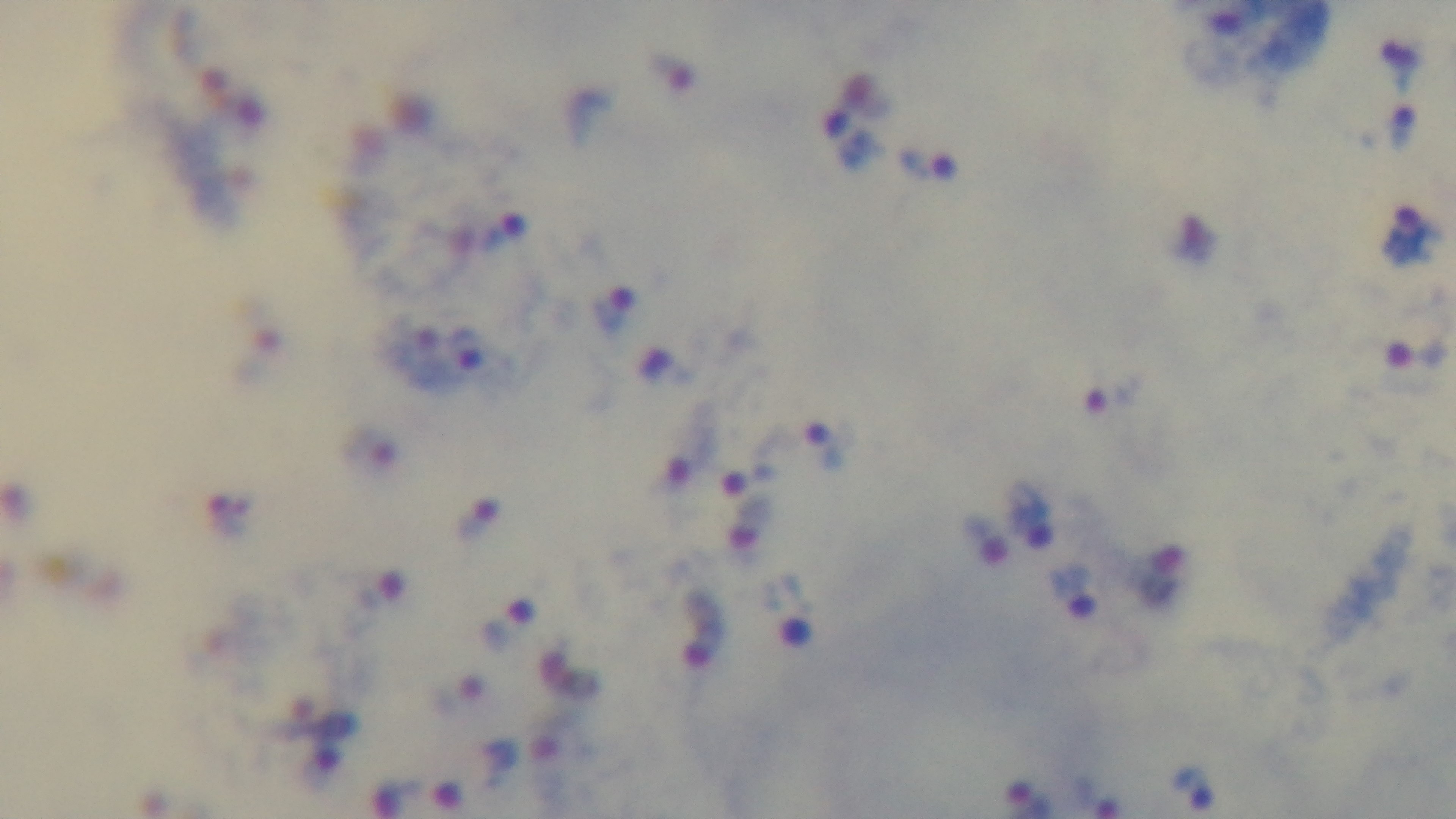
stain: Giemsa
preparation: thick smear
modality: light microscopy
malaria_status: infected
field_of_view: one from the slide
capture: mounted 4K digital camera
objective: 100x oil immersion